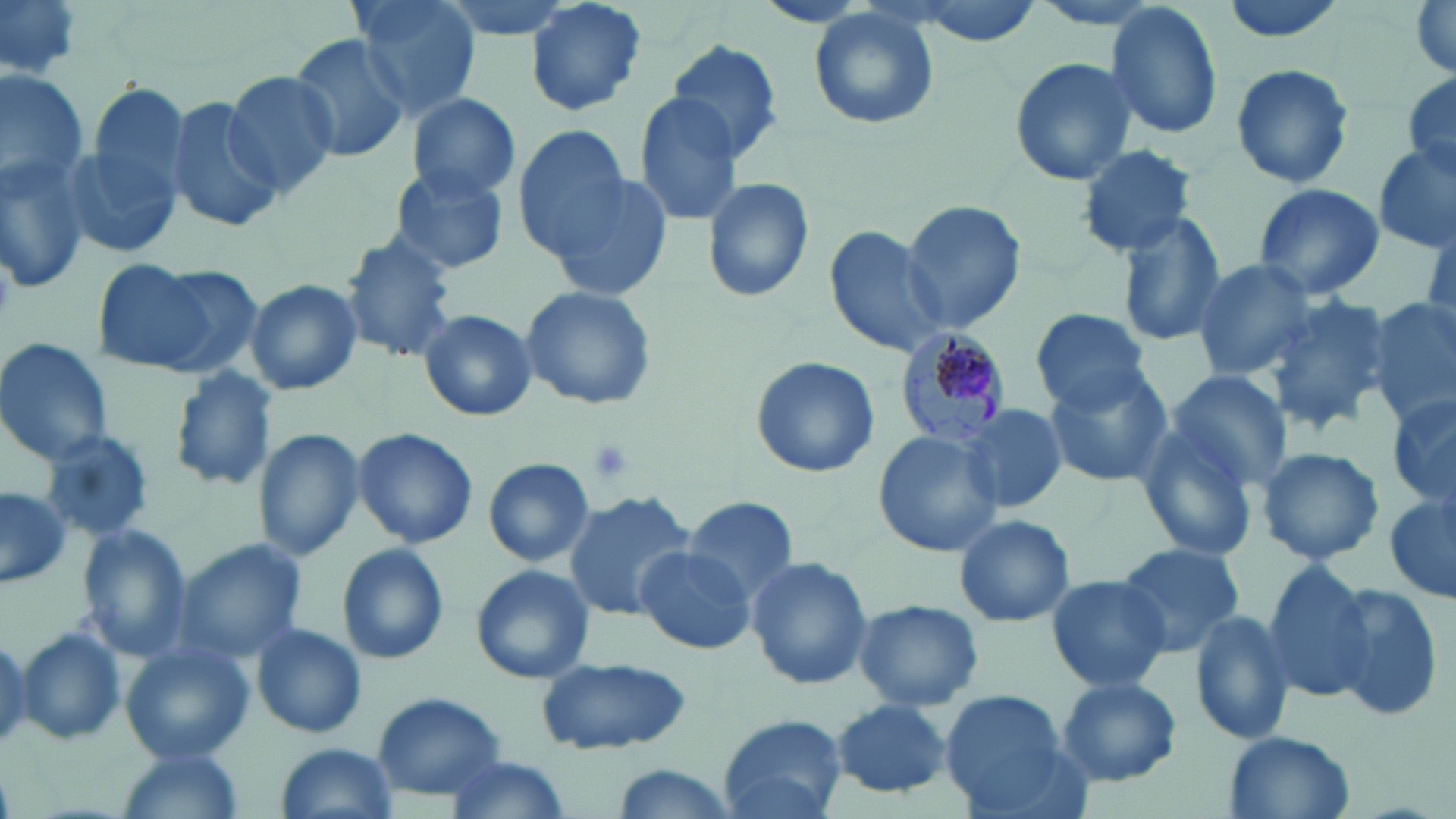
Summary:
  - Coordinate format: approximate bounding boxes as named x1/y1/x2/y2 corners in pixels
  - Platelet locations: (x1=582, y1=437, x2=637, y2=486)
  - Plasmodium malariae-infected red blood cell locations: (x1=894, y1=329, x2=1013, y2=446)
  - Uninfected red blood cell locations: (x1=0, y1=0, x2=83, y2=80), (x1=347, y1=0, x2=483, y2=122), (x1=430, y1=0, x2=584, y2=44), (x1=523, y1=0, x2=649, y2=118), (x1=898, y1=0, x2=1050, y2=44), (x1=1408, y1=0, x2=1455, y2=79), (x1=1103, y1=2, x2=1225, y2=141), (x1=808, y1=9, x2=940, y2=130), (x1=289, y1=32, x2=411, y2=165), (x1=662, y1=40, x2=786, y2=162), (x1=1009, y1=57, x2=1138, y2=187), (x1=1228, y1=62, x2=1355, y2=190), (x1=1, y1=69, x2=89, y2=194), (x1=224, y1=69, x2=337, y2=197), (x1=1401, y1=71, x2=1456, y2=183), (x1=86, y1=79, x2=192, y2=220), (x1=406, y1=92, x2=519, y2=200), (x1=164, y1=94, x2=285, y2=233), (x1=634, y1=94, x2=743, y2=227), (x1=514, y1=125, x2=630, y2=255), (x1=62, y1=132, x2=184, y2=264), (x1=1076, y1=144, x2=1200, y2=256), (x1=1373, y1=145, x2=1455, y2=255), (x1=0, y1=148, x2=94, y2=291), (x1=387, y1=164, x2=511, y2=276), (x1=549, y1=169, x2=673, y2=303), (x1=701, y1=176, x2=815, y2=305), (x1=1251, y1=183, x2=1385, y2=301), (x1=902, y1=199, x2=1025, y2=334), (x1=1117, y1=210, x2=1229, y2=347), (x1=825, y1=222, x2=948, y2=359), (x1=336, y1=234, x2=461, y2=364), (x1=92, y1=257, x2=241, y2=378), (x1=1192, y1=259, x2=1318, y2=381), (x1=243, y1=278, x2=364, y2=395), (x1=518, y1=286, x2=658, y2=411), (x1=1265, y1=295, x2=1394, y2=431), (x1=1368, y1=297, x2=1456, y2=424), (x1=417, y1=308, x2=538, y2=422), (x1=1031, y1=309, x2=1151, y2=414), (x1=0, y1=337, x2=115, y2=466), (x1=748, y1=355, x2=880, y2=478), (x1=168, y1=364, x2=280, y2=494), (x1=1041, y1=365, x2=1174, y2=488), (x1=1165, y1=368, x2=1292, y2=490), (x1=1387, y1=392, x2=1456, y2=512), (x1=958, y1=403, x2=1064, y2=514), (x1=1132, y1=422, x2=1263, y2=562), (x1=254, y1=426, x2=366, y2=561), (x1=351, y1=427, x2=478, y2=548), (x1=38, y1=429, x2=153, y2=542), (x1=873, y1=430, x2=1002, y2=558), (x1=1256, y1=446, x2=1385, y2=567), (x1=482, y1=458, x2=594, y2=567), (x1=0, y1=483, x2=72, y2=590), (x1=562, y1=490, x2=696, y2=620), (x1=1384, y1=490, x2=1456, y2=604), (x1=682, y1=496, x2=799, y2=606), (x1=953, y1=512, x2=1076, y2=628), (x1=76, y1=524, x2=194, y2=660), (x1=179, y1=540, x2=306, y2=658), (x1=1113, y1=541, x2=1245, y2=655), (x1=336, y1=543, x2=449, y2=666), (x1=633, y1=544, x2=757, y2=655), (x1=746, y1=557, x2=875, y2=689), (x1=1257, y1=559, x2=1379, y2=701), (x1=471, y1=564, x2=595, y2=684), (x1=1044, y1=573, x2=1172, y2=692), (x1=1328, y1=584, x2=1447, y2=725), (x1=853, y1=598, x2=983, y2=712), (x1=1189, y1=607, x2=1296, y2=746), (x1=252, y1=622, x2=367, y2=739), (x1=14, y1=625, x2=129, y2=749), (x1=0, y1=631, x2=35, y2=750), (x1=122, y1=642, x2=256, y2=766), (x1=535, y1=654, x2=695, y2=757), (x1=1057, y1=676, x2=1182, y2=786), (x1=371, y1=692, x2=507, y2=801), (x1=942, y1=693, x2=1073, y2=814), (x1=831, y1=699, x2=954, y2=798), (x1=718, y1=716, x2=846, y2=819), (x1=1222, y1=730, x2=1356, y2=819), (x1=276, y1=742, x2=397, y2=818), (x1=115, y1=747, x2=248, y2=819), (x1=437, y1=753, x2=572, y2=819), (x1=604, y1=765, x2=742, y2=818)
  - Slide-level diagnosis: Plasmodium malariae
  - Stain: May-Grünwald-Giemsa
  - Modality: light microscopy
  - Field of view: one of a larger specimen
  - Image size: 1456×819 pixels
  - Magnification: 1000x
  - Preparation: thin blood film